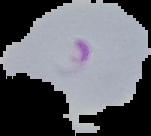 From a thin blood smear. Malaria status: parasitized. Image is 151×136 pixels. The area outside the segmented cell region is set to black.